Classify this cell by malaria status.
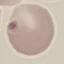

Uninfected.

Acquired by smartphone through the microscope eyepiece. Thin smear of blood. Giemsa-stained preparation. Cell patch, automatically extracted from a larger field of view and resized to 64 × 64 pixels.